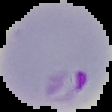 The area outside the segmented cell region is set to black. Image is 112×112 pixels. Result: malaria parasites detected. From a thin blood film.